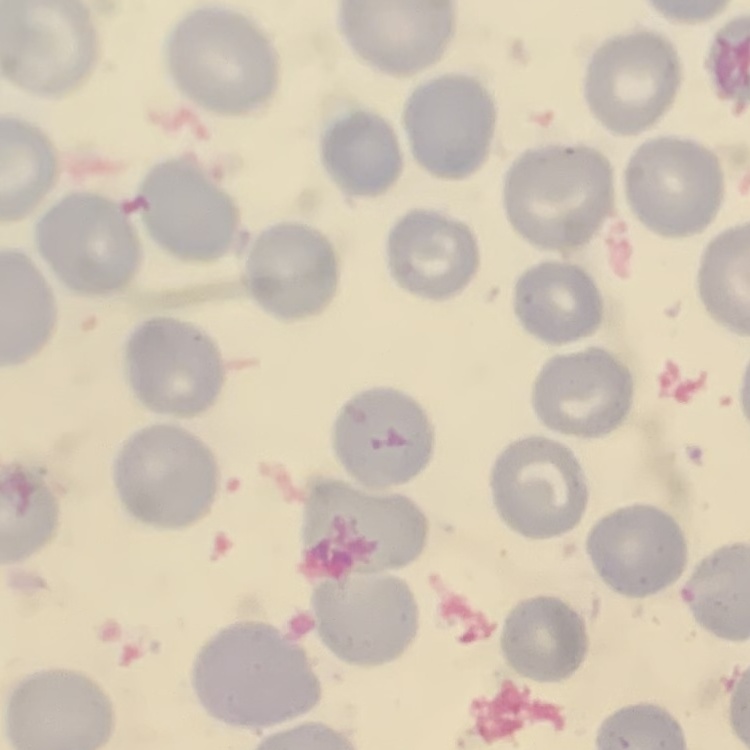
The red blood cells exhibit no rouleaux formation. Square crop of a larger photomicrograph. Stained with either Field's or Giemsa. Thin peripheral smear.